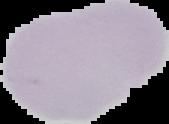 Result: no malaria parasites seen. From a thin blood film. Cell region segmented out of the field of view; the surrounding area is masked to black. Image is 169×124 pixels.